Classify this cell by malaria status.
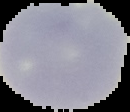
Uninfected.

From a thin blood smear. The area outside the segmented cell region is set to black. Image is 130×112 pixels.